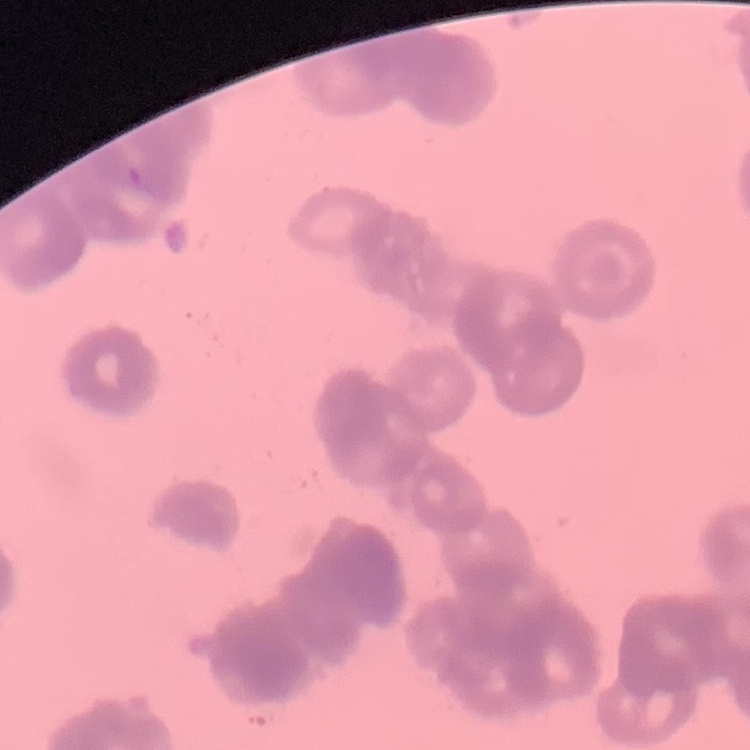
The erythrocytes exhibit rouleaux formation. Thin peripheral smear. One tile cut from a larger photomicrograph. Stained with either Field's or Giemsa.